Identify the parasite.
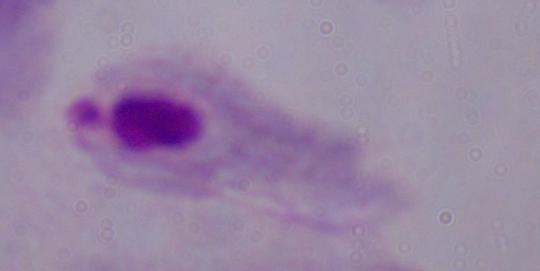
This is a trichomonad.

modality = photomicrograph
magnification = 1000x